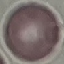
Malaria status: uninfected. Giemsa stain. Thin blood film. Cell patch, automatically extracted from a larger field of view and resized to 64 × 64 pixels. Photographed with a smartphone camera at the microscope eyepiece.